Locate every Babesia divergens-infected red blood cell.
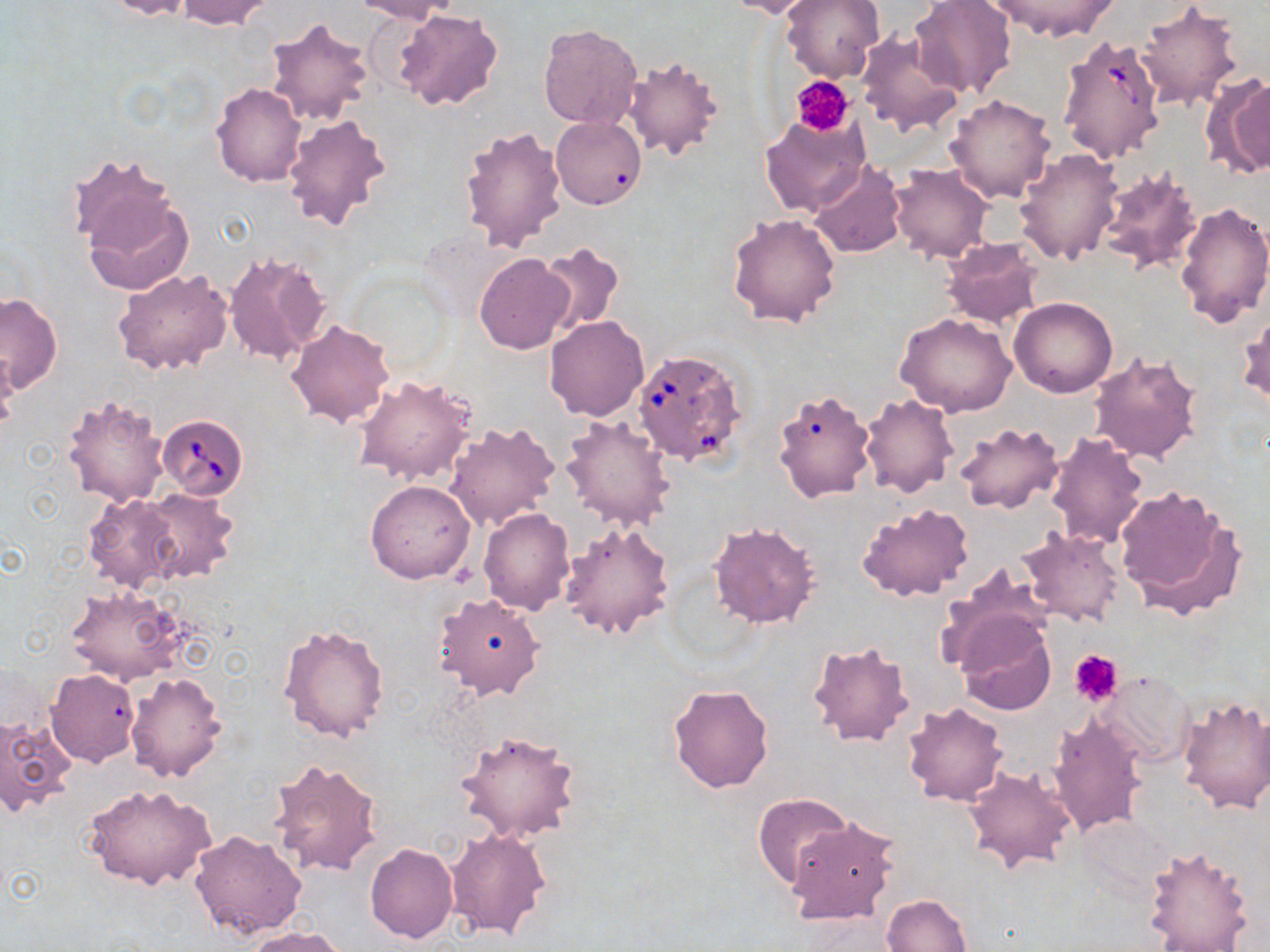
Approximate bounding boxes as (x1, y1, x2, y2) in pixels.
Babesia divergens-infected red blood cells: (1056, 34, 1170, 167), (633, 348, 748, 466), (157, 414, 249, 498).

Summary:
  - Uninfected red blood cell locations: (102, 0, 199, 20), (174, 0, 276, 29), (352, 0, 460, 23), (721, 0, 822, 19), (780, 0, 885, 82), (909, 0, 1018, 101), (984, 0, 1117, 42), (1135, 3, 1245, 111), (393, 8, 504, 112), (264, 15, 376, 128), (538, 22, 642, 129), (856, 30, 967, 139), (622, 53, 727, 160), (1200, 71, 1270, 181), (211, 82, 306, 186), (944, 94, 1056, 204), (282, 112, 393, 232), (759, 112, 871, 218), (552, 117, 645, 209), (458, 123, 568, 251), (1014, 149, 1123, 267), (70, 157, 191, 294), (809, 161, 905, 258), (888, 164, 994, 264), (1094, 167, 1206, 276), (1173, 199, 1270, 326), (726, 212, 842, 327), (939, 238, 1045, 328), (535, 242, 626, 335), (223, 249, 334, 367), (474, 252, 576, 354), (113, 268, 234, 377), (0, 292, 62, 392), (1008, 296, 1118, 398), (1238, 309, 1269, 412), (895, 312, 1019, 417), (544, 316, 650, 421), (286, 319, 396, 427), (1088, 349, 1205, 464), (0, 350, 20, 432), (354, 374, 477, 485), (771, 387, 876, 504), (61, 392, 168, 508), (859, 393, 959, 498), (559, 415, 676, 531), (444, 421, 560, 530), (952, 421, 1064, 515), (1045, 431, 1148, 549), (364, 480, 475, 584), (1114, 484, 1246, 617), (135, 488, 240, 584), (81, 492, 184, 594), (857, 501, 974, 602), (480, 507, 576, 615), (559, 520, 675, 639), (707, 520, 821, 629), (1018, 527, 1126, 628), (948, 540, 1120, 647), (936, 565, 1052, 673), (64, 584, 195, 686), (433, 591, 545, 700), (954, 613, 1057, 716), (277, 623, 390, 744), (805, 638, 917, 747), (45, 668, 140, 766), (124, 671, 227, 782), (1098, 671, 1195, 768), (667, 682, 776, 794), (1177, 693, 1270, 815), (902, 700, 1009, 806), (1046, 713, 1147, 838), (0, 715, 75, 817), (452, 727, 582, 845), (266, 757, 385, 878), (962, 762, 1078, 874), (84, 782, 215, 891), (753, 794, 852, 888), (783, 814, 900, 925), (1074, 814, 1173, 898), (446, 827, 552, 939), (189, 829, 308, 939), (365, 842, 458, 943), (1142, 845, 1254, 951), (881, 893, 972, 952), (243, 927, 348, 952)
  - Platelet locations: (792, 76, 854, 135), (1070, 649, 1124, 706)
  - Slide-level diagnosis: Babesia divergens
  - Magnification: 1000x
  - Field of view: one of a larger specimen
  - Preparation: thin blood smear
  - Stain: May-Grünwald-Giemsa
  - Image size: 1270×952 pixels
  - Modality: light microscopy